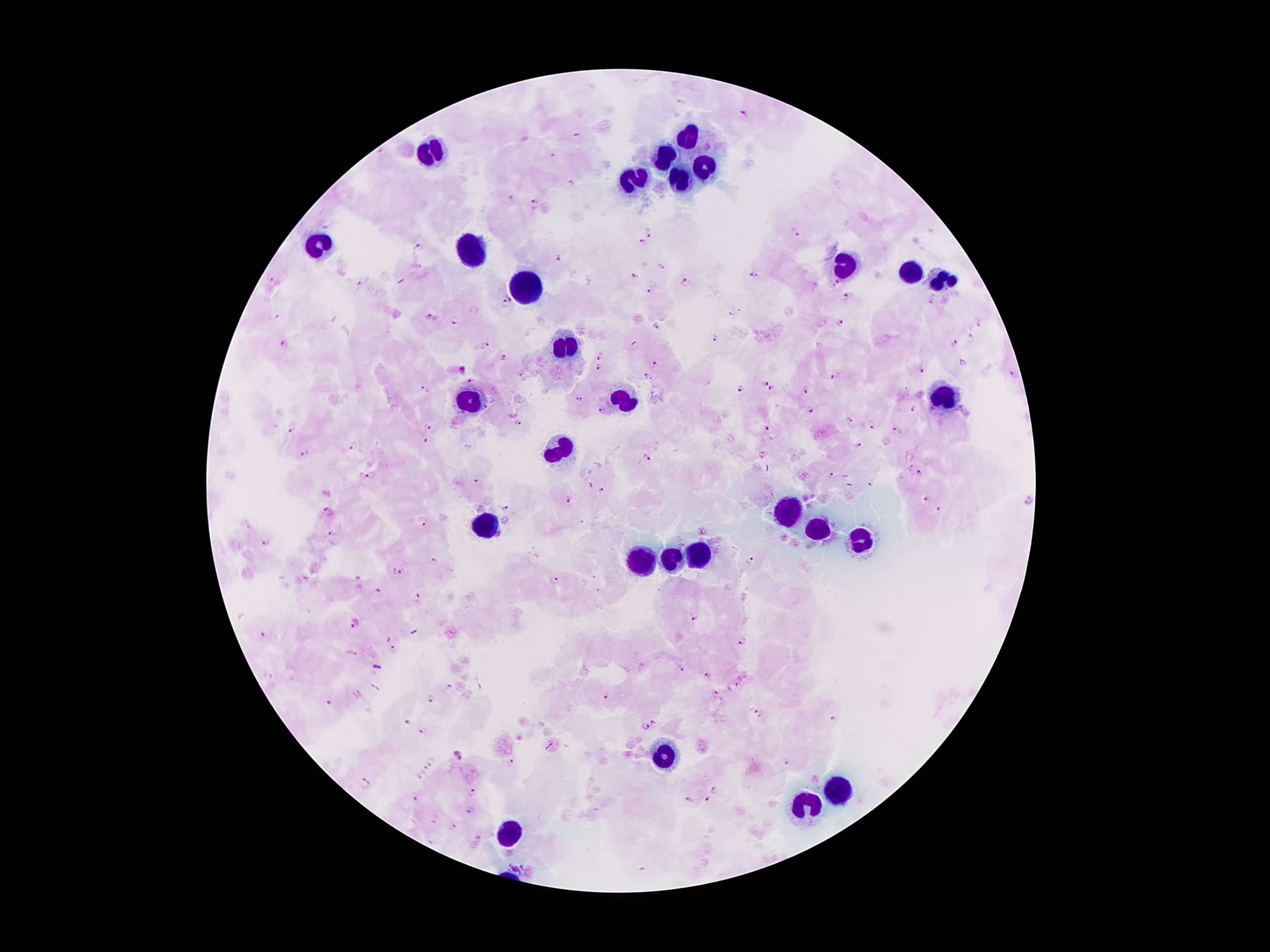

Approximate centers as {x, y} in pixels. Leukocyte locations: {688, 139}, {433, 151}, {667, 156}, {704, 166}, {636, 177}, {683, 180}, {320, 246}, {468, 251}, {846, 269}, {913, 275}, {940, 280}, {523, 290}, {564, 346}, {940, 399}, {473, 403}, {619, 403}, {559, 450}, {785, 514}, {485, 525}, {816, 532}, {698, 558}, {641, 562}, {674, 562}, {664, 754}, {840, 791}, {806, 806}, {510, 832}. Malaria parasite locations: {745, 113}, {576, 134}, {551, 155}, {572, 180}, {511, 197}, {534, 201}, {648, 233}, {797, 235}, {642, 243}, {419, 247}, {558, 258}, {660, 267}, {634, 275}, {754, 275}, {270, 278}, {686, 281}, {838, 281}, {360, 283}, {833, 286}, {650, 290}, {847, 295}, {510, 298}, {930, 302}, {505, 304}, {731, 313}, {431, 318}, {454, 321}, {840, 322}, {978, 324}, {657, 327}, {716, 339}, {955, 343}, {285, 344}, {485, 345}, {601, 356}, {503, 358}, {962, 363}, {654, 364}, {599, 369}, {463, 370}, {923, 371}, {1014, 373}, {648, 377}, {835, 377}, {470, 381}, {765, 383}, {424, 389}, {772, 389}, {741, 390}, {805, 390}, {576, 398}, {581, 400}, {494, 401}, {485, 407}, {811, 410}, {913, 410}, {602, 411}, {850, 420}, {520, 424}, {427, 425}, {871, 425}, {293, 428}, {766, 428}, {899, 431}, {426, 440}, {857, 445}, {354, 446}, {304, 453}, {763, 455}, {648, 458}, {910, 467}, {921, 474}, {372, 475}, {832, 475}, {478, 483}, {589, 486}, {601, 492}, {926, 500}, {569, 501}, {1029, 501}, {504, 509}, {940, 510}, {327, 513}, {423, 522}, {332, 535}, {266, 544}, {435, 561}, {750, 561}, {394, 572}, {402, 572}, {357, 578}, {555, 582}, {378, 590}, {599, 590}, {418, 598}, {693, 616}, {355, 623}, {261, 635}, {742, 640}, {393, 649}, {679, 669}, {708, 676}, {448, 687}, {715, 694}, {605, 696}, {431, 699}, {327, 702}, {753, 712}, {762, 717}, {833, 718}, {406, 722}, {656, 723}, {645, 727}, {425, 731}, {458, 755}, {432, 761}, {783, 761}, {509, 763}, {427, 769}, {416, 776}, {366, 783}, {715, 791}, {473, 793}, {415, 798}, {707, 800}, {687, 801}, {469, 809}, {453, 828}, {475, 838}. 100x magnification. Thick peripheral-blood smear. Single field of view. Patient malaria status: positive for Plasmodium falciparum. Image is 1270×952 pixels. Photographed through the microscope eyepiece with a smartphone camera. Giemsa stain.